State which parasite is depicted.
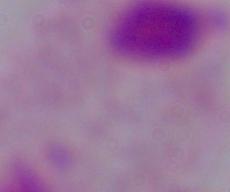
This is a trichomonad.

Summary:
  - Modality: micrograph
  - Magnification: 1000x